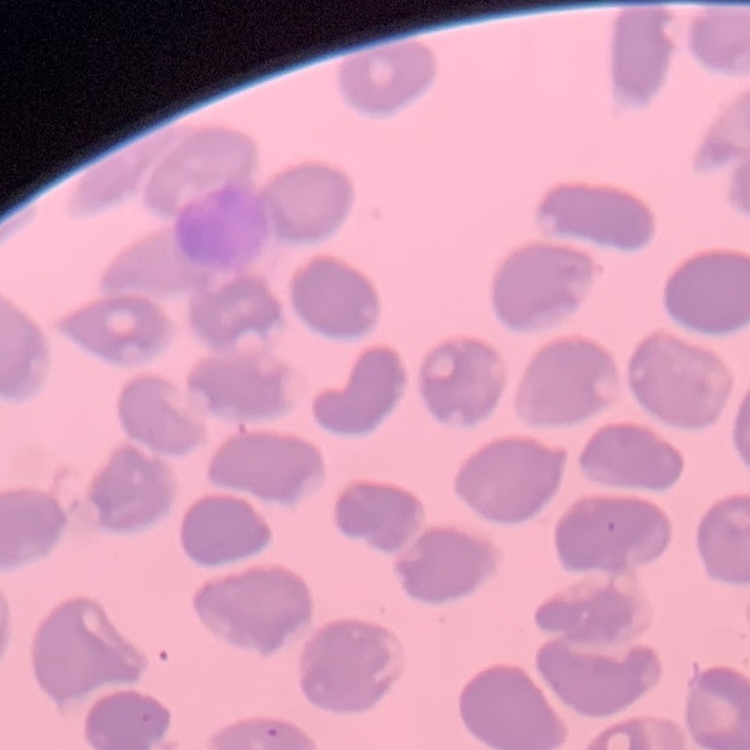

erythrocyte morphology = no rouleaux formation
preparation = thin peripheral smear
stain = Field's or Giemsa
image type = one tile cut from a larger photomicrograph